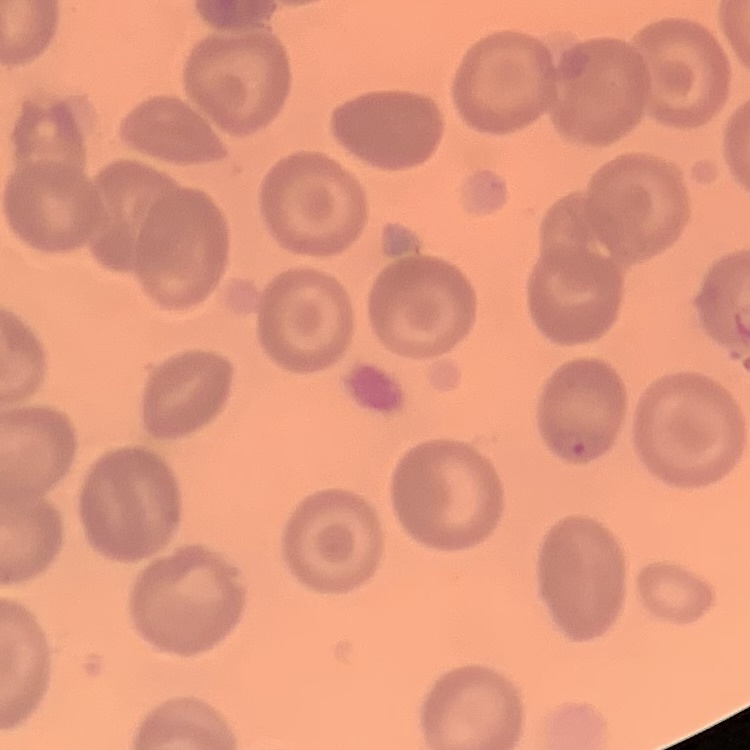

Summary:
  - Erythrocyte morphology: no rouleaux formation
  - Preparation: thin blood film
  - Stain: Field's or Giemsa
  - Image type: square crop of a larger photomicrograph